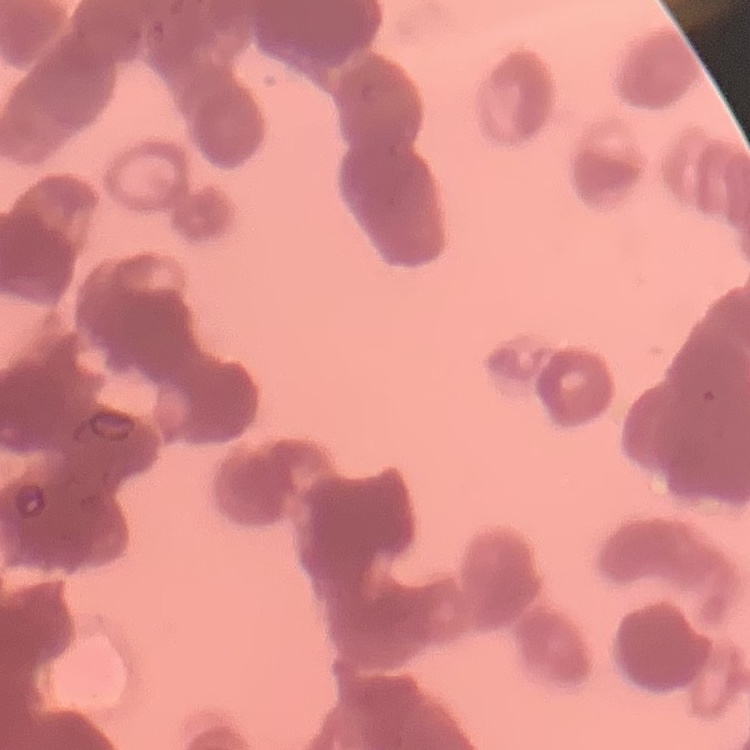

Summary:
  - Erythrocyte morphology: rouleaux formation
  - Preparation: thin blood smear
  - Image type: square crop of a larger photomicrograph
  - Stain: Field's or Giemsa